Describe the morphology of the erythrocytes.
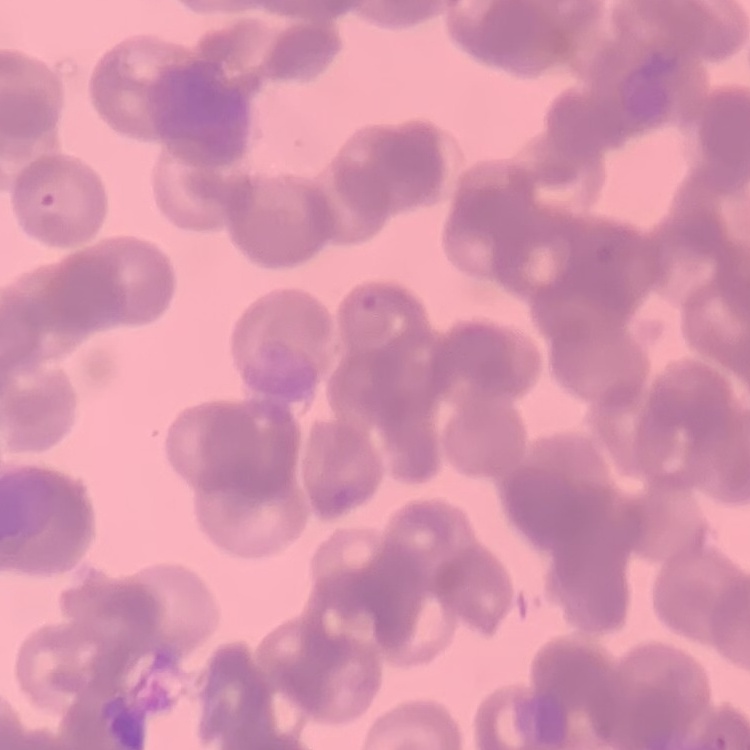

They show rouleaux formation.

Field's or Giemsa stain. Thin peripheral smear. Square crop of a larger photomicrograph.